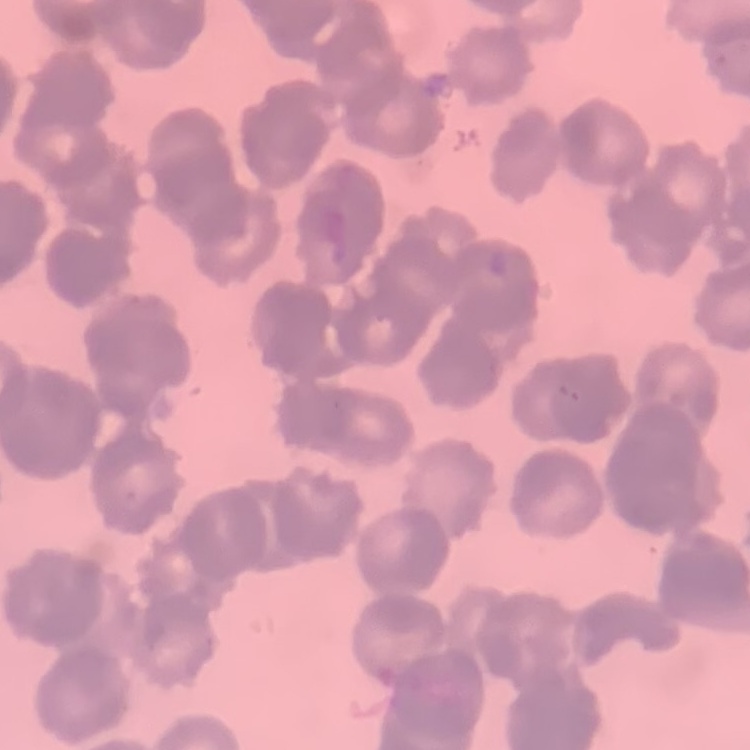

{
  "red_blood_cell_morphology": "rouleaux formation",
  "preparation": "thin blood film",
  "stain": "Field's or Giemsa",
  "image_type": "one tile cut from a larger photomicrograph"
}